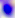

Toxoplasma gondii is shown. Micrograph. Captured at 400x magnification.